Assess this cell for malaria.
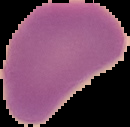
It is uninfected.

From a thin blood smear. Image is 130×127 pixels. Cell region segmented out of the field of view; the surrounding area is masked to black.